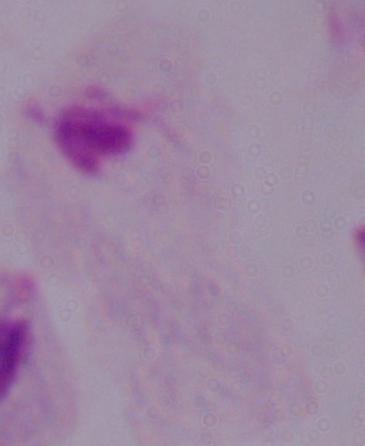
Micrograph. Captured at 1000x magnification. A trichomonad is shown.